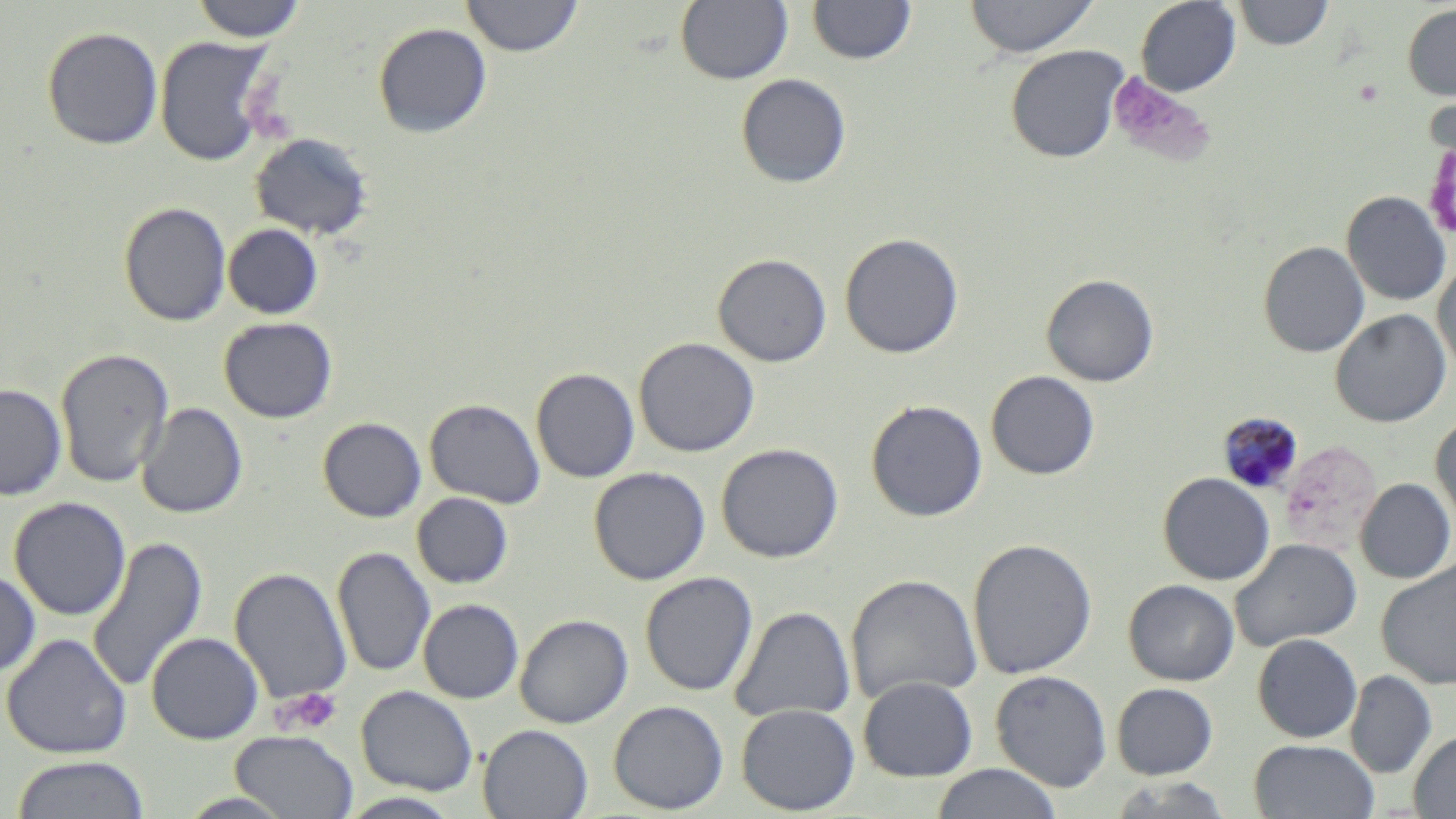
{
  "slide_level_diagnosis": "Plasmodium malariae",
  "platelet_locations": "approximate bounding boxes as [x1, y1, x2, y2] in pixels: [1108, 73, 1207, 164], [271, 688, 344, 736]",
  "field_of_view": "one of a larger specimen",
  "magnification": "1000x",
  "plasmodium_malariae_infected_red_blood_cell_locations": "approximate bounding boxes as [x1, y1, x2, y2] in pixels: [1217, 410, 1303, 492]",
  "stain": "May-Grünwald-Giemsa",
  "uninfected_red_blood_cell_locations": "approximate bounding boxes as [x1, y1, x2, y2] in pixels: [191, 0, 308, 43], [461, 0, 583, 57], [964, 0, 1099, 58], [1136, 0, 1241, 96], [675, 1, 794, 85], [807, 1, 917, 66], [1234, 1, 1333, 50], [1402, 3, 1456, 101], [373, 22, 492, 138], [42, 26, 163, 150], [155, 35, 275, 166], [1006, 44, 1129, 163], [735, 74, 852, 189], [1422, 113, 1456, 249], [249, 132, 374, 240], [1341, 191, 1451, 306], [118, 201, 232, 327], [223, 223, 323, 319], [839, 232, 964, 358], [1258, 240, 1370, 357], [713, 253, 832, 366], [1433, 261, 1456, 378], [1041, 273, 1159, 386], [1330, 309, 1451, 427], [219, 317, 337, 422], [633, 337, 760, 457], [55, 348, 174, 487], [531, 367, 640, 483], [986, 370, 1100, 480], [0, 383, 66, 500], [425, 398, 546, 508], [866, 399, 988, 521], [137, 403, 248, 519], [1430, 415, 1456, 530], [318, 416, 426, 522], [716, 443, 843, 563], [589, 466, 711, 585], [1157, 472, 1275, 586], [1356, 478, 1455, 583], [412, 492, 513, 588], [8, 496, 131, 621], [87, 535, 209, 694], [967, 538, 1097, 679], [1229, 538, 1361, 652], [332, 546, 436, 676], [1376, 559, 1456, 690], [229, 567, 352, 705], [0, 570, 41, 678], [639, 571, 759, 696], [845, 574, 982, 706], [1123, 579, 1239, 685], [418, 598, 524, 704], [730, 606, 855, 724], [515, 614, 633, 728], [146, 632, 264, 745], [1, 633, 131, 759], [1253, 633, 1362, 743], [1345, 669, 1437, 778], [990, 670, 1112, 792], [857, 675, 978, 781], [1111, 683, 1218, 779], [356, 686, 478, 796], [608, 700, 729, 814], [736, 703, 859, 815], [477, 724, 593, 819], [1409, 730, 1456, 818], [231, 731, 358, 818], [1249, 738, 1378, 819], [10, 755, 149, 819], [929, 764, 1062, 819], [1104, 775, 1235, 818], [337, 792, 464, 818]",
  "preparation": "thin blood film",
  "image_size": "1456×819 pixels",
  "modality": "optical microscopy"
}